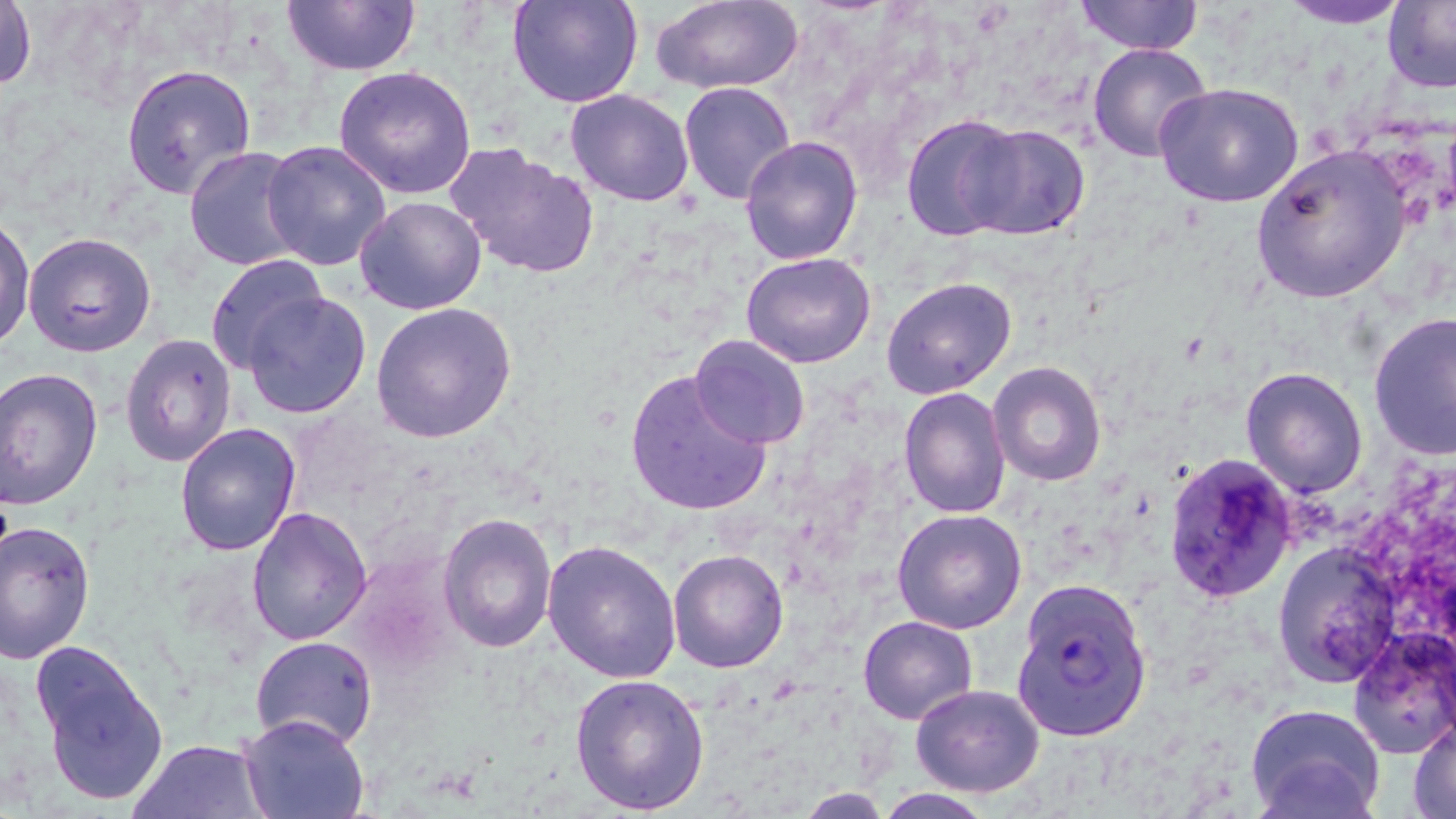
Summary:
  - Coordinate format: approximate bounding boxes as (x1, y1, x2, y2) in pixels
  - Plasmodium falciparum-infected red blood cell locations: (1013, 579, 1153, 743)
  - Platelet locations: (1219, 482, 1272, 548)
  - Uninfected red blood cell locations: (280, 0, 423, 77), (506, 0, 643, 108), (1075, 0, 1201, 54), (1281, 0, 1411, 27), (1, 1, 37, 96), (648, 1, 804, 92), (1382, 1, 1454, 90), (1088, 42, 1213, 163), (121, 64, 257, 198), (333, 66, 478, 199), (678, 80, 795, 203), (1154, 84, 1304, 209), (565, 88, 696, 206), (901, 117, 1029, 239), (959, 123, 1089, 240), (739, 135, 863, 266), (261, 140, 393, 271), (1251, 143, 1411, 305), (447, 144, 596, 278), (183, 147, 309, 270), (355, 195, 487, 315), (0, 215, 35, 353), (24, 231, 157, 357), (203, 252, 325, 372), (741, 252, 877, 368), (883, 276, 1016, 397), (243, 292, 371, 420), (371, 302, 518, 445), (1368, 312, 1456, 458), (120, 332, 236, 469), (689, 335, 810, 449), (989, 361, 1106, 484), (0, 367, 103, 509), (623, 367, 774, 518), (1241, 367, 1368, 497), (899, 387, 1010, 518), (175, 422, 303, 556), (1162, 454, 1296, 602), (246, 506, 373, 646), (892, 508, 1028, 632), (438, 511, 557, 652), (0, 520, 96, 663), (543, 540, 681, 682), (1275, 544, 1398, 683), (668, 549, 789, 673), (859, 616, 978, 724), (1348, 627, 1456, 757), (251, 636, 377, 749), (30, 642, 169, 810), (570, 673, 712, 815), (911, 685, 1044, 797), (1244, 703, 1387, 819), (239, 714, 367, 818), (1410, 718, 1456, 817), (130, 737, 267, 819)
  - Slide-level diagnosis: Plasmodium falciparum
  - Stain: May-Grünwald-Giemsa
  - Magnification: 1000x
  - Image size: 1456×819 pixels
  - Modality: light microscopy
  - Field of view: one of a larger specimen
  - Preparation: thin blood film